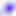
magnification = 400x
modality = micrograph
identification = Toxoplasma gondii